Point out each malaria parasite and each leukocyte.
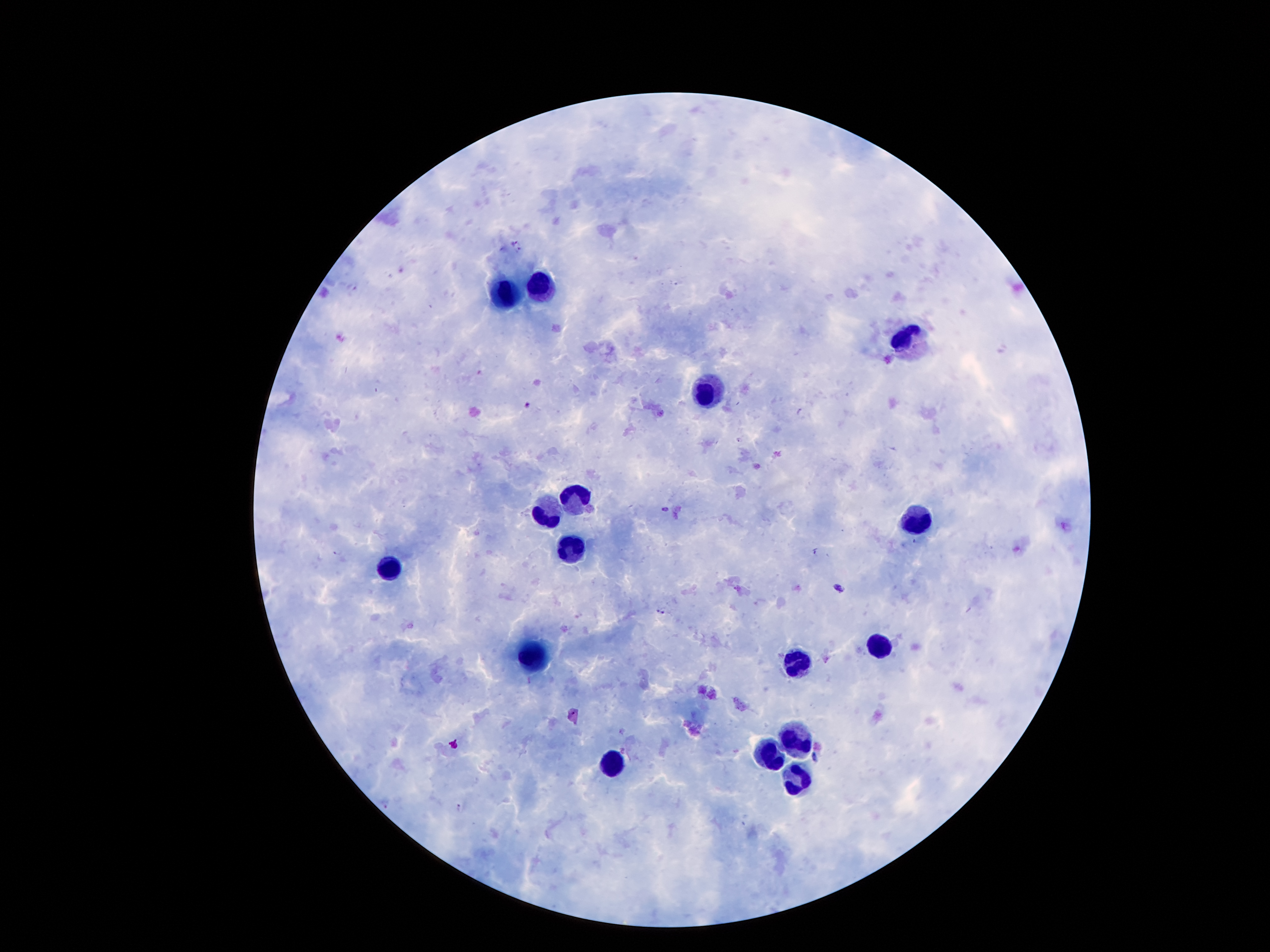

Approximate object centers, in pixels from the top-left corner.
Malaria parasites: (x=517, y=240), (x=519, y=248), (x=800, y=411), (x=666, y=509), (x=816, y=554), (x=839, y=588), (x=662, y=611), (x=815, y=759), (x=456, y=807).
Leukocytes: (x=537, y=289), (x=501, y=295), (x=903, y=345), (x=704, y=387), (x=579, y=502), (x=546, y=514), (x=922, y=516), (x=574, y=550), (x=387, y=565), (x=877, y=644), (x=534, y=657), (x=793, y=661), (x=791, y=744), (x=770, y=753), (x=611, y=763), (x=795, y=781).

Giemsa-stained preparation. 100x magnification. Thick blood smear. Single field of view. Image is 1270×952 pixels. Patient malaria status: positive for Plasmodium falciparum. Smartphone photograph taken through the microscope eyepiece.